Outline each Trypanosoma brucei.
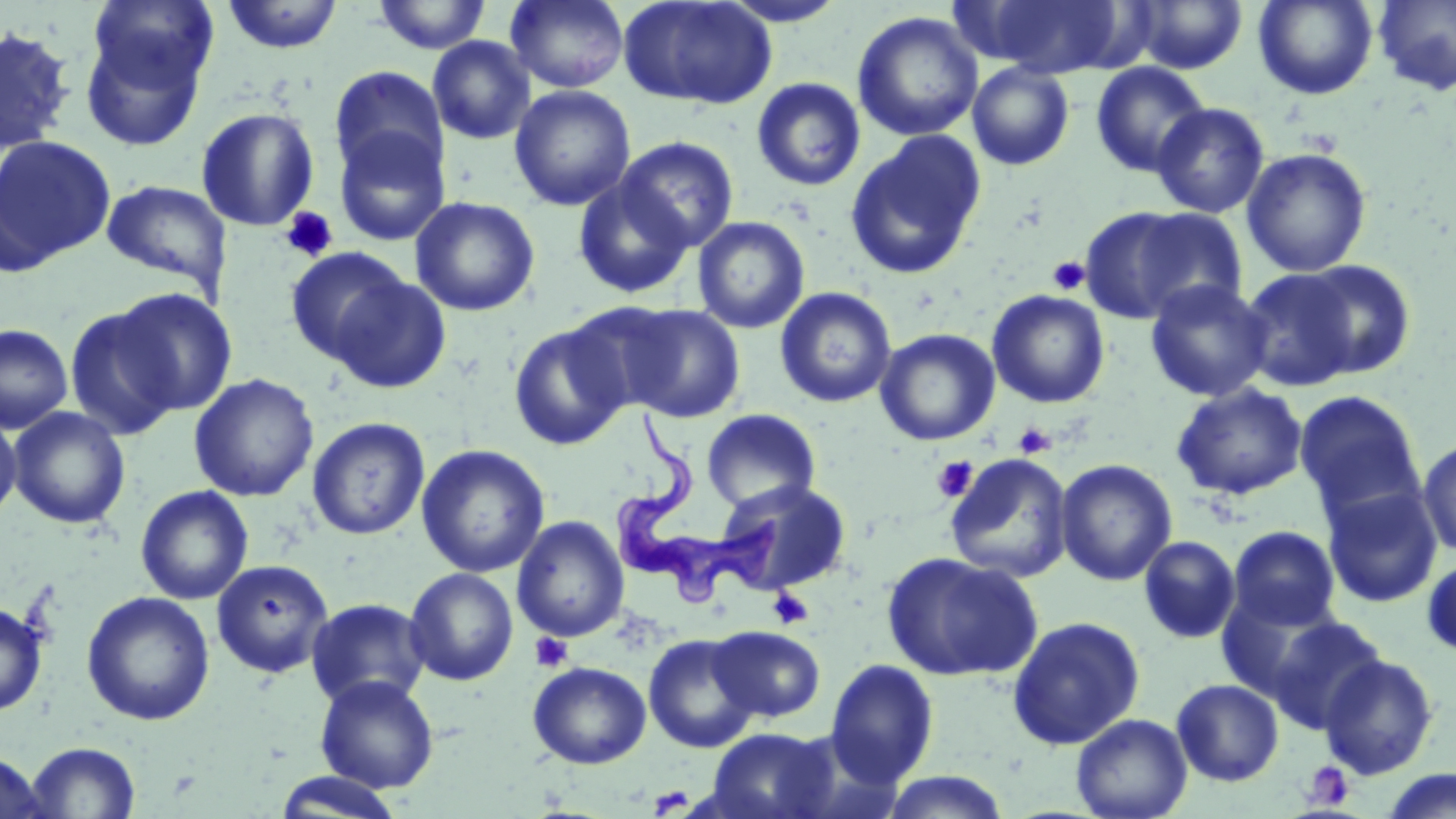

Approximate bounding boxes as (x1,y1)-(x2,y2) corner pairs in pixels.
Trypanosoma brucei: (608,409)-(782,603).

Summary:
  - Platelet locations: (280,207)-(339,263), (1047,256)-(1090,295), (1013,422)-(1056,458), (932,456)-(978,502), (768,588)-(814,629), (529,632)-(574,672), (1303,760)-(1355,810)
  - Uninfected red blood cell locations: (369,0)-(493,54), (505,0)-(630,93), (717,0)-(850,27), (983,0)-(1128,77), (1127,0)-(1248,74), (1253,0)-(1379,100), (1373,0)-(1456,96), (220,1)-(345,55), (619,1)-(777,111), (851,11)-(983,142), (76,17)-(210,147), (0,25)-(77,154), (427,36)-(536,144), (1090,61)-(1211,178), (967,62)-(1075,170), (329,65)-(449,181), (752,77)-(865,191), (509,84)-(636,211), (1151,102)-(1269,218), (195,107)-(320,232), (332,126)-(451,246), (844,130)-(987,280), (0,135)-(116,270), (615,136)-(739,253), (1241,148)-(1372,277), (572,178)-(694,299), (101,180)-(231,290), (410,196)-(541,316), (1079,206)-(1229,326), (692,216)-(810,334), (285,247)-(411,364), (1294,259)-(1417,378), (1238,267)-(1364,391), (327,272)-(452,395), (1145,280)-(1273,402), (112,287)-(237,415), (774,287)-(897,408), (987,289)-(1110,408), (564,300)-(686,413), (619,304)-(746,422), (63,305)-(184,440), (508,321)-(631,450), (0,324)-(73,434), (875,328)-(1000,446), (189,373)-(319,502), (1171,383)-(1308,500), (1293,390)-(1425,522), (8,406)-(130,529), (701,408)-(821,513), (0,412)-(22,523), (307,417)-(430,540), (1417,438)-(1456,558), (416,444)-(550,578), (944,453)-(1074,583), (1055,459)-(1178,586), (715,478)-(851,595), (135,485)-(254,604), (1322,485)-(1443,608), (512,515)-(629,642), (1228,526)-(1341,631), (1138,535)-(1241,644), (881,551)-(1042,682), (1421,554)-(1456,660), (211,558)-(334,678), (404,567)-(519,686), (1217,589)-(1346,703), (80,591)-(216,726), (305,598)-(431,709), (0,600)-(48,717), (1262,614)-(1389,734), (1006,615)-(1146,750), (709,627)-(826,721), (643,633)-(761,753), (1318,653)-(1439,780), (824,659)-(940,787), (527,661)-(651,769), (314,675)-(439,792), (1171,679)-(1284,786), (1071,713)-(1192,819), (704,727)-(841,819), (25,741)-(142,818), (0,752)-(49,818), (1378,769)-(1456,819), (876,771)-(1013,818), (273,772)-(406,818)
  - Slide-level diagnosis: Trypanosoma brucei
  - Preparation: thin blood smear
  - Stain: May-Grünwald-Giemsa
  - Field of view: single
  - Modality: optical microscopy
  - Magnification: 1000x
  - Image size: 1456×819 pixels